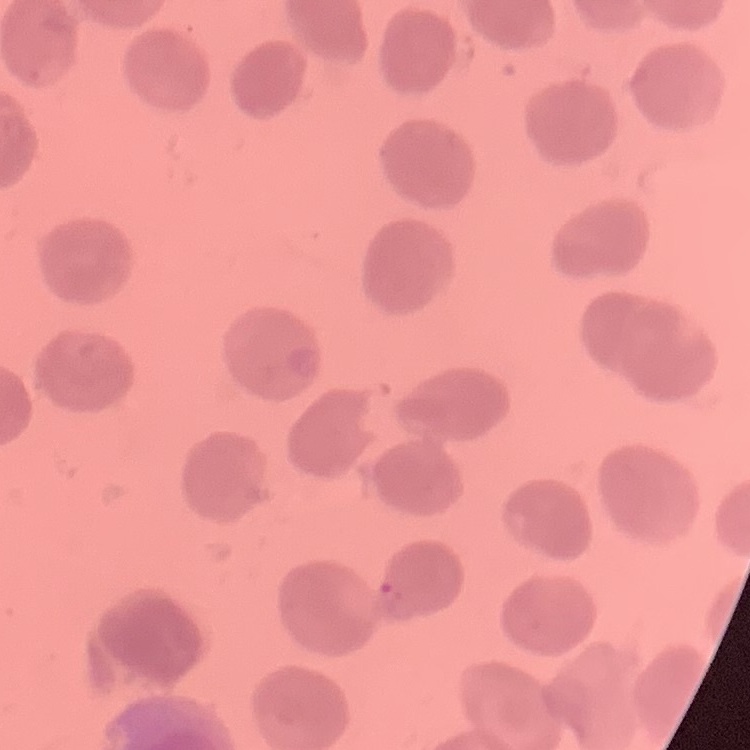
The erythrocytes exhibit no rouleaux formation. Square crop of a larger photomicrograph. Thin peripheral smear. Field's or Giemsa stain.